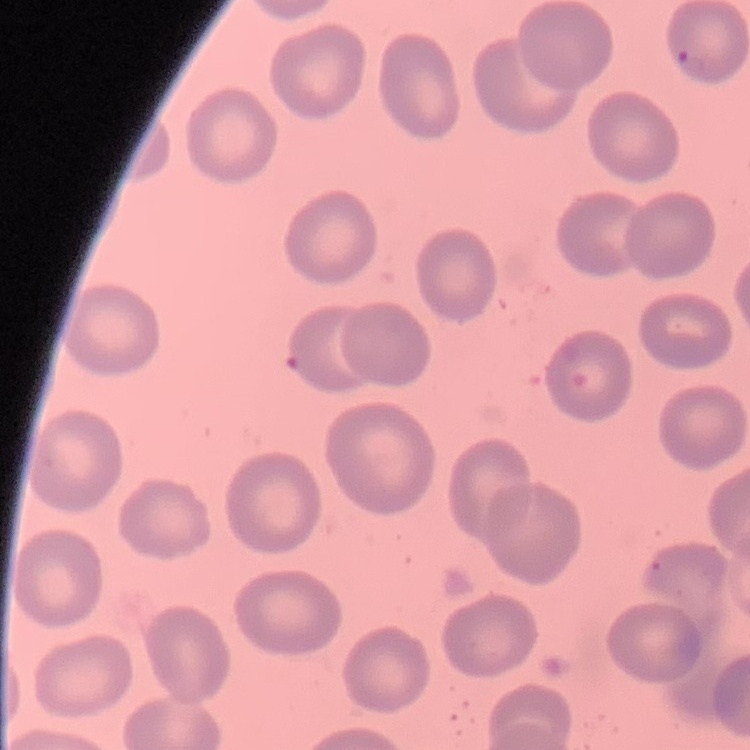
red blood cell morphology = no rouleaux formation
stain = Field's or Giemsa
preparation = thin peripheral smear
image type = one tile cut from a larger photomicrograph